Locate every blood parasite and identify its species.
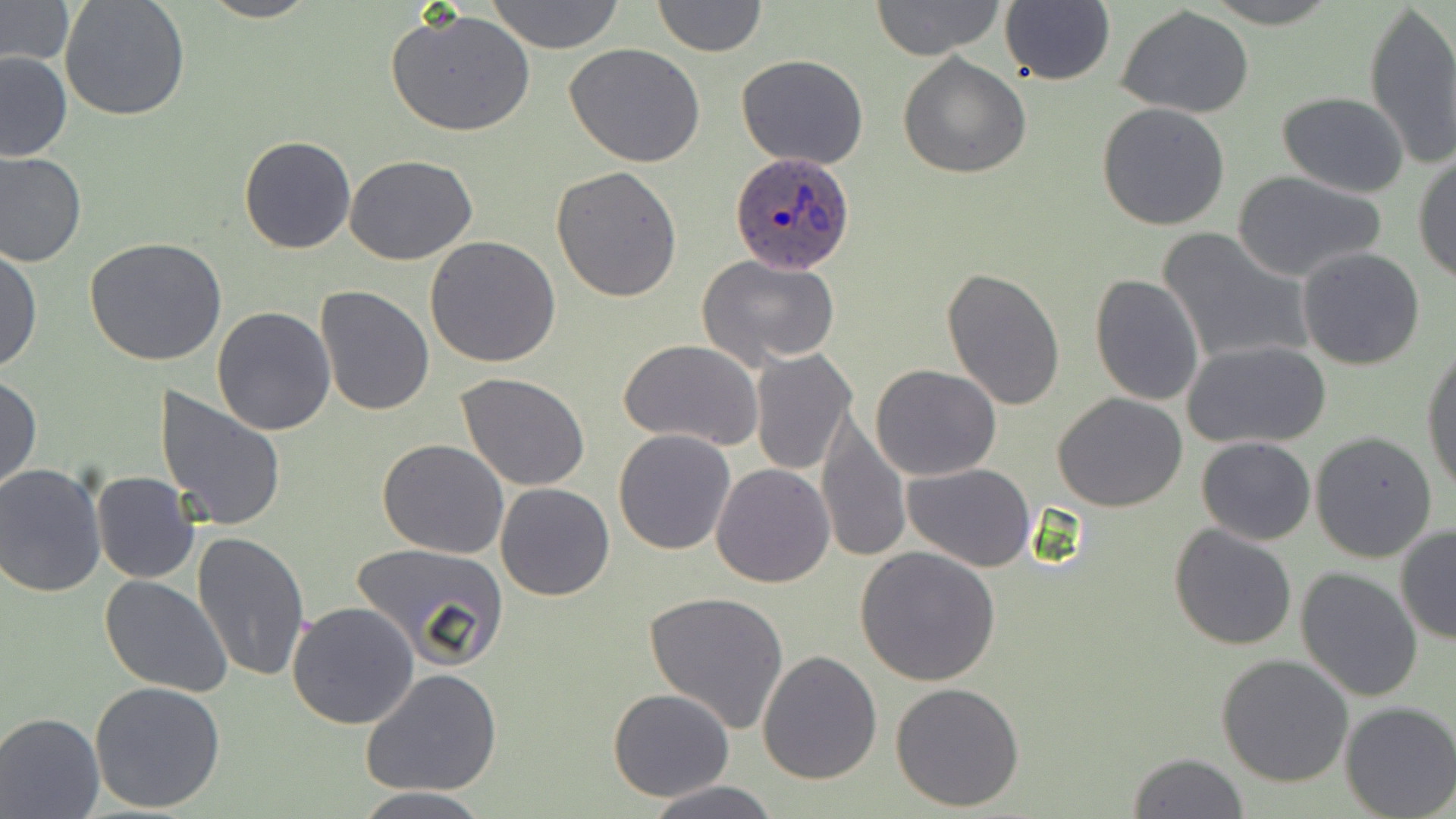

Approximate bounding boxes as (x1,y1)-(x2,y2) corner pairs in pixels.
Plasmodium ovale-infected red blood cells: (730,151)-(854,274).
No Plasmodium falciparum, Plasmodium malariae, Plasmodium vivax, Babesia divergens, or Trypanosoma brucei observed.

Uninfected red blood cell locations: (0,0)-(74,64), (61,0)-(190,123), (197,0)-(319,23), (485,0)-(626,52), (650,0)-(767,56), (870,0)-(1007,61), (1000,0)-(1116,87), (1202,0)-(1341,27), (1363,0)-(1456,169), (1117,5)-(1255,119), (387,9)-(537,138), (566,44)-(706,168), (0,48)-(72,161), (736,54)-(869,171), (898,54)-(1030,178), (1277,92)-(1409,197), (1096,102)-(1231,230), (239,137)-(356,254), (0,149)-(87,266), (1414,152)-(1456,286), (344,154)-(478,266), (550,165)-(683,303), (1230,170)-(1391,281), (1158,226)-(1313,368), (424,235)-(561,368), (83,238)-(229,367), (1,245)-(41,376), (1295,245)-(1425,370), (695,253)-(841,372), (940,268)-(1066,409), (1089,274)-(1206,406), (316,285)-(435,414), (211,306)-(335,435), (620,339)-(763,452), (1185,340)-(1331,449), (1422,341)-(1455,494), (750,348)-(856,474), (868,364)-(1001,481), (457,372)-(591,493), (1,375)-(42,493), (154,387)-(287,535), (1052,392)-(1189,512), (815,413)-(910,566), (613,429)-(738,555), (1310,431)-(1439,562), (1196,437)-(1317,545), (377,438)-(509,557), (0,462)-(107,598), (904,462)-(1035,570), (711,464)-(834,587), (91,471)-(199,584), (495,483)-(615,601), (1168,522)-(1297,649), (1395,525)-(1456,645), (191,529)-(312,682), (352,542)-(509,670), (857,547)-(1000,685), (1295,567)-(1423,702), (100,576)-(232,696), (644,590)-(789,733), (286,601)-(419,730), (757,650)-(882,785), (1216,654)-(1355,789), (360,667)-(503,798), (88,680)-(226,812), (890,682)-(1025,812), (608,688)-(735,802), (1339,701)-(1456,818), (0,712)-(104,818), (1125,750)-(1250,818), (642,781)-(783,818), (352,788)-(494,818). Slide-level diagnosis: Plasmodium ovale. May-Grünwald-Giemsa-stained preparation. 1000x magnification. One field of a larger specimen. Light microscopy. Thin blood film. Image is 1456×819 pixels.